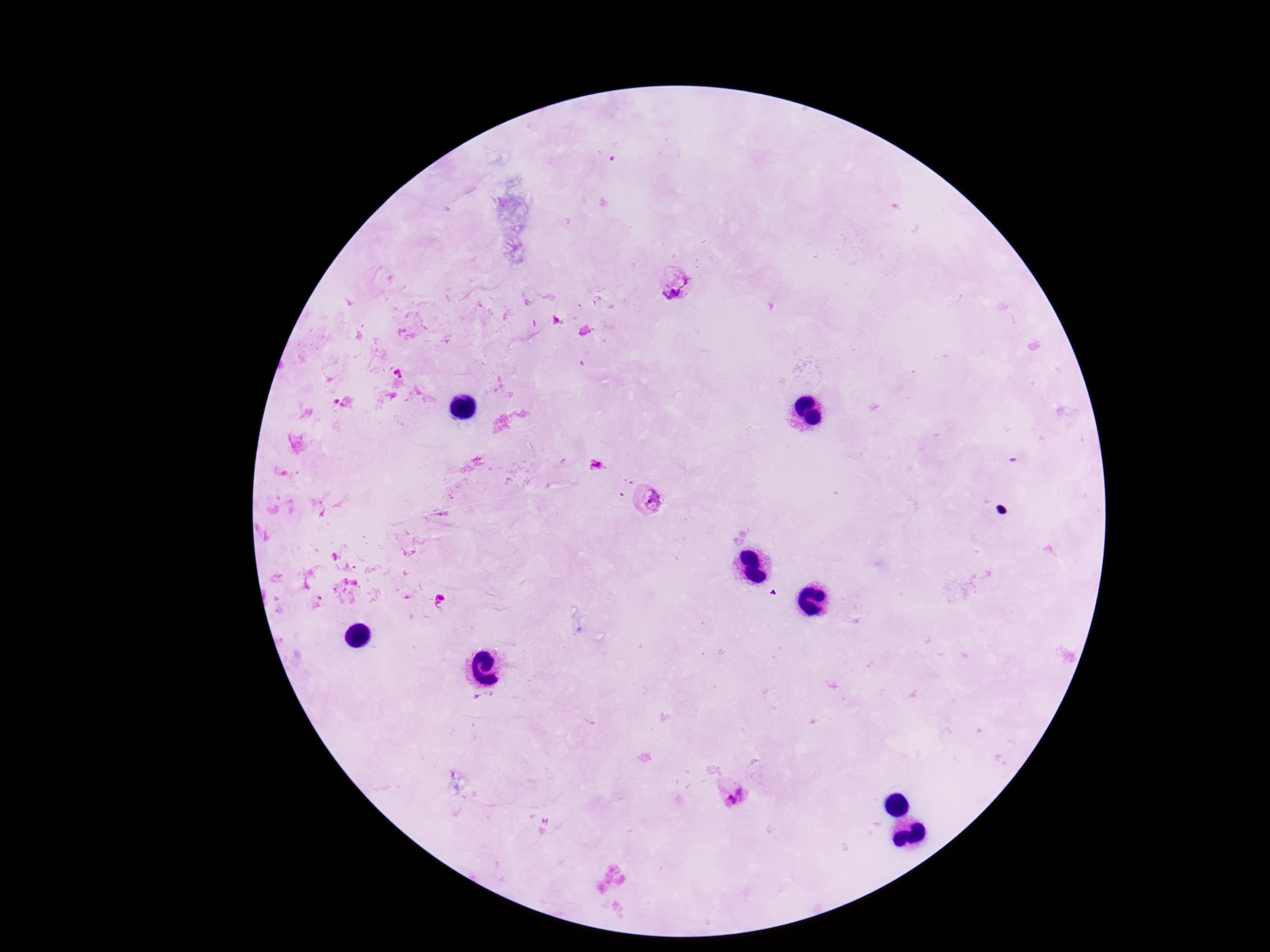

Approximate object centers, in pixels from the top-left corner. Plasmodium parasite locations: (x=676, y=283), (x=597, y=465), (x=645, y=502), (x=730, y=798). Image is 1270×952 pixels. One field from this slide. Photographed through the microscope eyepiece with a smartphone camera. Giemsa-stained preparation. Patient malaria status: positive. 100x magnification. Thick blood film.